Find the red blood cells that are infected with P. falciparum, and any of indeterminate infection status.
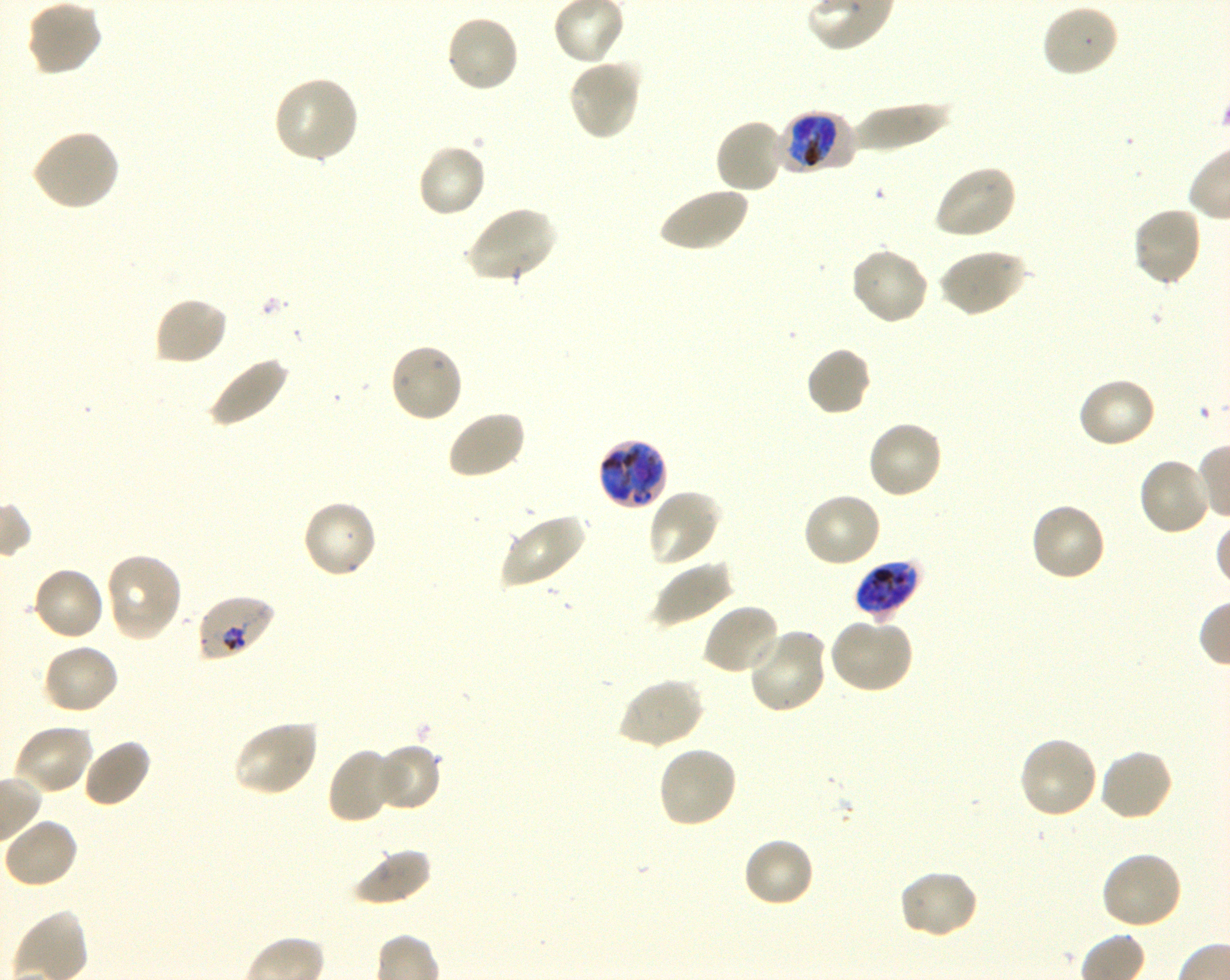
Approximate bounding rectangles given as corner coordinates in pixels from the top-left. Not every red blood cell is marked. A life-cycle stage — or a range of stages, where the recorded stages span more than one — follows each staged infected red blood cell.
Infected red blood cells: (x1=779, y1=111, x2=846, y2=173) early trophozoite to early schizont; (x1=596, y1=437, x2=668, y2=511) early trophozoite to early schizont; (x1=854, y1=560, x2=922, y2=618) late trophozoite to late schizont; (x1=196, y1=595, x2=277, y2=663) trophozoite.
No red blood cells of indeterminate infection status observed.

Locations of uninfected red blood cells: (x1=25, y1=0, x2=102, y2=78), (x1=1040, y1=4, x2=1120, y2=79), (x1=444, y1=13, x2=521, y2=94), (x1=567, y1=58, x2=642, y2=142), (x1=273, y1=76, x2=361, y2=164), (x1=850, y1=100, x2=951, y2=153), (x1=714, y1=117, x2=787, y2=195), (x1=30, y1=128, x2=121, y2=212), (x1=415, y1=143, x2=487, y2=220), (x1=932, y1=163, x2=1017, y2=240), (x1=656, y1=185, x2=749, y2=253), (x1=466, y1=206, x2=557, y2=285), (x1=1131, y1=206, x2=1203, y2=287), (x1=850, y1=246, x2=929, y2=326), (x1=939, y1=248, x2=1027, y2=317), (x1=152, y1=295, x2=229, y2=367), (x1=388, y1=342, x2=465, y2=424), (x1=805, y1=345, x2=873, y2=417), (x1=206, y1=354, x2=291, y2=429), (x1=1075, y1=376, x2=1158, y2=451), (x1=444, y1=408, x2=527, y2=481), (x1=866, y1=420, x2=945, y2=500), (x1=1136, y1=455, x2=1213, y2=536), (x1=646, y1=487, x2=723, y2=568), (x1=800, y1=491, x2=883, y2=569), (x1=300, y1=499, x2=377, y2=579), (x1=1028, y1=502, x2=1107, y2=583), (x1=500, y1=512, x2=589, y2=588), (x1=105, y1=553, x2=183, y2=642), (x1=651, y1=559, x2=733, y2=627), (x1=32, y1=565, x2=106, y2=642), (x1=701, y1=602, x2=782, y2=677), (x1=828, y1=618, x2=914, y2=695), (x1=746, y1=627, x2=830, y2=714), (x1=41, y1=642, x2=121, y2=716), (x1=616, y1=677, x2=704, y2=751), (x1=232, y1=719, x2=320, y2=797), (x1=12, y1=722, x2=94, y2=798), (x1=1017, y1=736, x2=1099, y2=821), (x1=81, y1=737, x2=152, y2=809), (x1=374, y1=743, x2=440, y2=813), (x1=657, y1=746, x2=738, y2=830), (x1=326, y1=748, x2=403, y2=823), (x1=1097, y1=748, x2=1175, y2=824), (x1=4, y1=819, x2=80, y2=889), (x1=741, y1=836, x2=816, y2=909), (x1=349, y1=846, x2=433, y2=907), (x1=1098, y1=850, x2=1183, y2=931), (x1=897, y1=868, x2=980, y2=941). Oil immersion, 100x objective (numerical aperture 1.30). Giemsa-stained preparation. One field from this slide. Donor blood group O+. Image is 1230×980 pixels. P. falciparum strain 3D7 in shaking in-vitro culture. Thin blood smear.